Identify the cell.
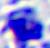
A leukocyte.

modality: micrograph
magnification: 400x